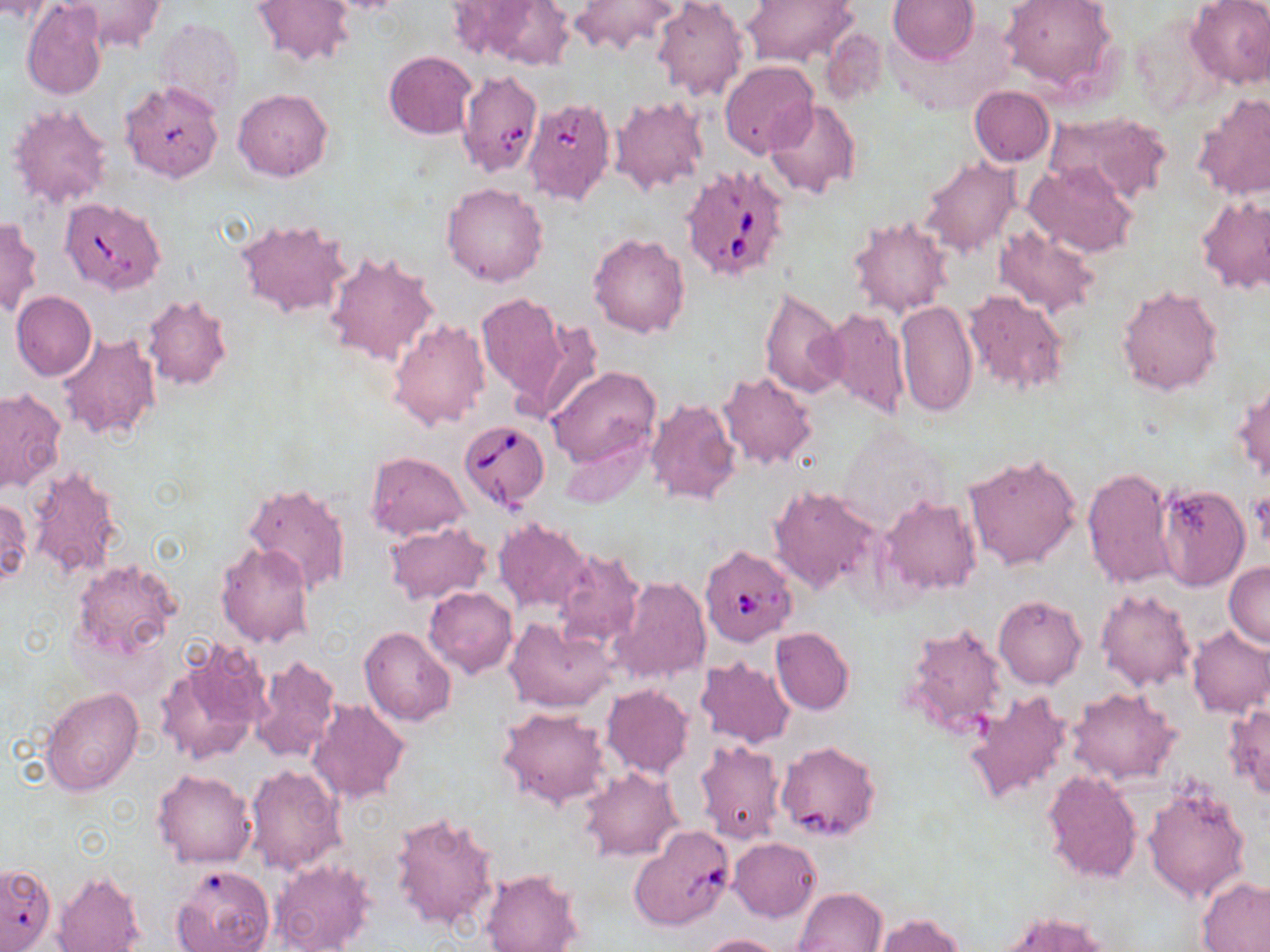
Approximate bounding boxes as named x1/y1/x2/y2 corners in pixels. Uninfected red blood cell locations: (x1=0, y1=0, x2=54, y2=23), (x1=63, y1=0, x2=166, y2=52), (x1=250, y1=0, x2=355, y2=69), (x1=318, y1=0, x2=412, y2=14), (x1=653, y1=0, x2=750, y2=102), (x1=742, y1=0, x2=860, y2=68), (x1=888, y1=0, x2=979, y2=65), (x1=999, y1=0, x2=1117, y2=91), (x1=1185, y1=0, x2=1270, y2=90), (x1=22, y1=2, x2=108, y2=100), (x1=469, y1=2, x2=577, y2=70), (x1=569, y1=2, x2=683, y2=57), (x1=154, y1=18, x2=243, y2=117), (x1=820, y1=26, x2=888, y2=109), (x1=383, y1=51, x2=476, y2=138), (x1=719, y1=61, x2=818, y2=157), (x1=120, y1=82, x2=225, y2=184), (x1=970, y1=86, x2=1054, y2=166), (x1=233, y1=88, x2=332, y2=182), (x1=1192, y1=92, x2=1270, y2=202), (x1=611, y1=96, x2=709, y2=194), (x1=765, y1=98, x2=862, y2=200), (x1=6, y1=102, x2=112, y2=210), (x1=1043, y1=111, x2=1172, y2=202), (x1=919, y1=158, x2=1021, y2=258), (x1=1025, y1=161, x2=1138, y2=258), (x1=442, y1=182, x2=549, y2=287), (x1=1196, y1=195, x2=1269, y2=294), (x1=847, y1=214, x2=952, y2=318), (x1=0, y1=216, x2=41, y2=317), (x1=235, y1=218, x2=353, y2=317), (x1=992, y1=224, x2=1102, y2=319), (x1=589, y1=232, x2=690, y2=338), (x1=325, y1=251, x2=439, y2=367), (x1=1116, y1=285, x2=1223, y2=396), (x1=759, y1=286, x2=845, y2=399), (x1=962, y1=290, x2=1068, y2=395), (x1=12, y1=291, x2=96, y2=382), (x1=476, y1=291, x2=571, y2=409), (x1=141, y1=295, x2=232, y2=392), (x1=896, y1=298, x2=978, y2=419), (x1=822, y1=306, x2=908, y2=419), (x1=388, y1=318, x2=490, y2=431), (x1=520, y1=319, x2=605, y2=425), (x1=57, y1=332, x2=160, y2=443), (x1=548, y1=365, x2=660, y2=467), (x1=717, y1=371, x2=819, y2=470), (x1=1232, y1=379, x2=1270, y2=483), (x1=0, y1=386, x2=66, y2=493), (x1=642, y1=394, x2=739, y2=502), (x1=837, y1=427, x2=951, y2=532), (x1=560, y1=431, x2=654, y2=508), (x1=366, y1=451, x2=469, y2=540), (x1=963, y1=454, x2=1084, y2=571), (x1=24, y1=464, x2=125, y2=580), (x1=1081, y1=466, x2=1179, y2=591), (x1=243, y1=483, x2=350, y2=594), (x1=1155, y1=484, x2=1249, y2=591), (x1=769, y1=485, x2=882, y2=596), (x1=880, y1=496, x2=980, y2=596), (x1=0, y1=497, x2=32, y2=587), (x1=493, y1=519, x2=591, y2=613), (x1=383, y1=522, x2=491, y2=605), (x1=216, y1=543, x2=314, y2=649), (x1=550, y1=550, x2=645, y2=650), (x1=71, y1=559, x2=181, y2=665), (x1=1224, y1=562, x2=1270, y2=649), (x1=610, y1=576, x2=711, y2=685), (x1=424, y1=586, x2=518, y2=678), (x1=1095, y1=588, x2=1197, y2=692), (x1=993, y1=594, x2=1087, y2=689), (x1=504, y1=618, x2=617, y2=713), (x1=899, y1=622, x2=1009, y2=742), (x1=1186, y1=626, x2=1270, y2=718), (x1=359, y1=627, x2=456, y2=726), (x1=771, y1=628, x2=855, y2=714), (x1=155, y1=640, x2=270, y2=768), (x1=251, y1=654, x2=340, y2=763), (x1=328, y1=654, x2=434, y2=783), (x1=695, y1=658, x2=795, y2=746), (x1=602, y1=684, x2=694, y2=777), (x1=40, y1=686, x2=142, y2=797), (x1=965, y1=688, x2=1073, y2=807), (x1=1067, y1=688, x2=1179, y2=784), (x1=306, y1=699, x2=410, y2=805), (x1=1225, y1=702, x2=1270, y2=799), (x1=497, y1=707, x2=611, y2=809), (x1=692, y1=739, x2=786, y2=844), (x1=776, y1=744, x2=878, y2=843), (x1=244, y1=764, x2=346, y2=873), (x1=579, y1=768, x2=680, y2=861), (x1=1042, y1=769, x2=1143, y2=883), (x1=152, y1=770, x2=257, y2=869), (x1=1141, y1=782, x2=1251, y2=903), (x1=390, y1=810, x2=498, y2=931), (x1=728, y1=838, x2=820, y2=922), (x1=270, y1=858, x2=375, y2=952), (x1=171, y1=864, x2=275, y2=952), (x1=480, y1=870, x2=582, y2=952), (x1=54, y1=872, x2=145, y2=952), (x1=1197, y1=876, x2=1270, y2=951), (x1=795, y1=887, x2=887, y2=952), (x1=993, y1=912, x2=1113, y2=952), (x1=876, y1=913, x2=964, y2=952), (x1=698, y1=934, x2=784, y2=952). Babesia divergens-infected red blood cell locations: (x1=451, y1=68, x2=535, y2=178), (x1=523, y1=97, x2=616, y2=209), (x1=680, y1=164, x2=794, y2=282), (x1=54, y1=196, x2=167, y2=295), (x1=459, y1=420, x2=550, y2=512), (x1=692, y1=536, x2=799, y2=645), (x1=630, y1=826, x2=736, y2=931). Slide-level diagnosis: Babesia divergens. May-Grünwald-Giemsa stain. 1000x magnification. Light microscopy. Thin blood smear. One field of a larger specimen. Image is 1270×952 pixels.